Assess this cell for malaria.
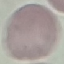

It is uninfected.

Summary:
  - Image type: automatically extracted cell patch, resized to 64 × 64 pixels
  - Preparation: thin blood smear
  - Stain: Giemsa
  - Capture: smartphone camera at the microscope eyepiece